Comment on the morphology of the erythrocytes.
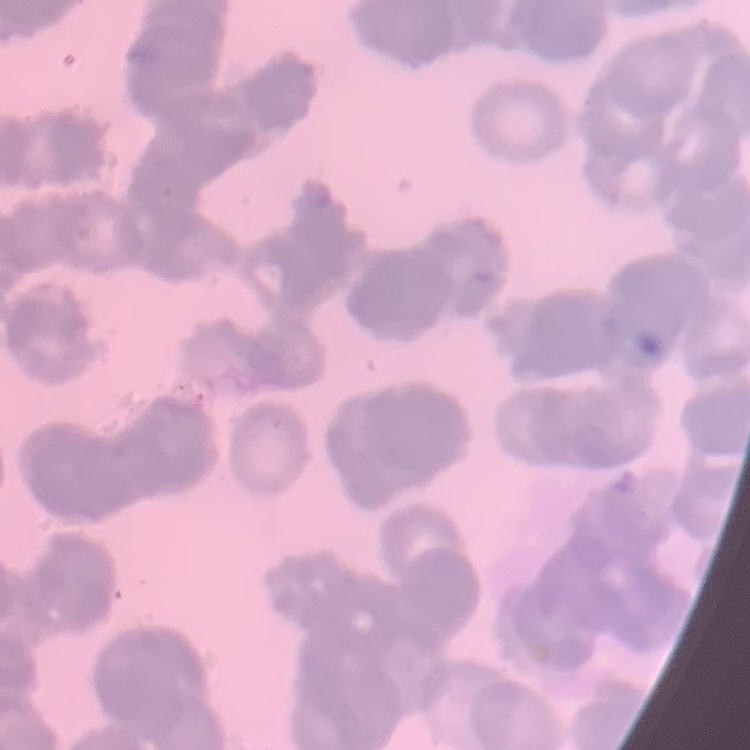

They show rouleaux formation.

image type = one tile cut from a larger photomicrograph
preparation = thin blood film
stain = Field's or Giemsa